Outline each blood parasite and name the species.
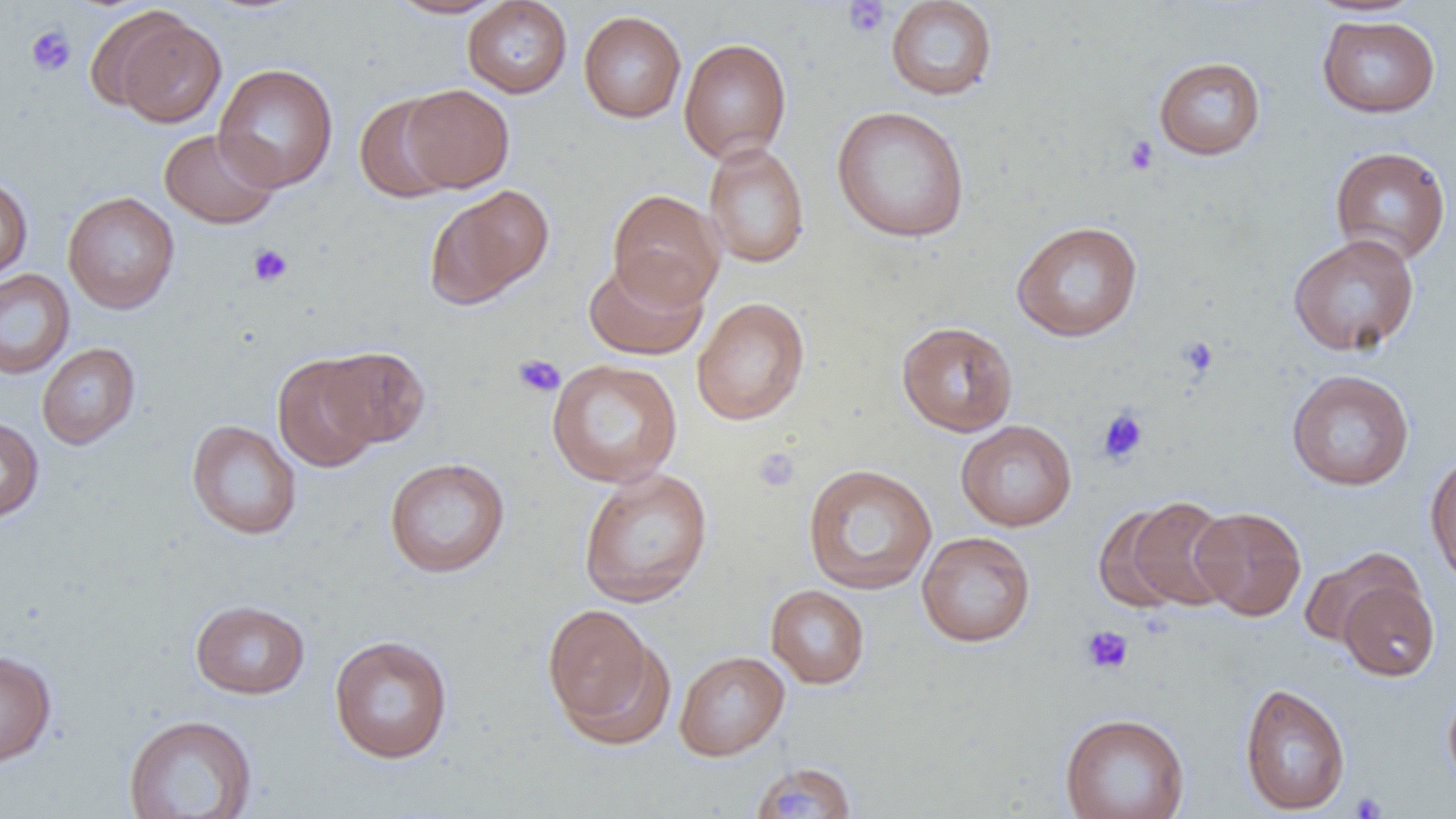
No blood parasites observed.

Summary:
  - Coordinate format: approximate bounding boxes as (x1,y1)-(x2,y2) corner pairs in pixels
  - Uninfected red blood cell locations: (385,0)-(509,19), (885,0)-(998,101), (462,1)-(572,98), (578,11)-(686,123), (111,14)-(226,128), (1317,15)-(1440,118), (678,37)-(793,163), (1153,56)-(1266,160), (213,63)-(338,192), (402,84)-(514,192), (354,92)-(459,203), (831,105)-(970,243), (159,127)-(281,229), (703,141)-(810,269), (1330,146)-(1451,265), (0,174)-(32,282), (426,184)-(555,308), (607,189)-(725,309), (62,191)-(179,315), (1011,220)-(1143,342), (1288,233)-(1420,357), (583,255)-(709,361), (0,269)-(75,380), (691,297)-(810,426), (896,320)-(1018,437), (37,343)-(140,450), (317,346)-(430,448), (272,353)-(383,472), (546,358)-(683,488), (1286,369)-(1415,491), (0,416)-(44,522), (186,420)-(302,540), (955,420)-(1077,531), (1424,452)-(1456,585), (384,457)-(510,578), (802,463)-(937,595), (577,467)-(714,608), (1106,495)-(1237,612), (1190,506)-(1307,620), (916,531)-(1036,647), (1298,547)-(1422,648), (1337,578)-(1440,681), (765,584)-(870,689), (190,599)-(311,699), (541,603)-(670,743), (328,635)-(453,764), (0,649)-(58,768), (674,650)-(790,761), (1442,681)-(1456,794), (1239,682)-(1351,815), (1059,712)-(1190,819), (123,713)-(257,818), (750,762)-(856,819)
  - Platelet locations: (843,0)-(890,38), (25,24)-(76,77), (1123,135)-(1158,176), (247,243)-(293,287), (1177,335)-(1219,379), (513,353)-(565,398), (1097,408)-(1149,465), (753,446)-(801,493), (1081,625)-(1134,675), (1349,791)-(1387,818)
  - Slide-level diagnosis: negative for blood parasites
  - Magnification: 1000x
  - Image size: 1456×819 pixels
  - Modality: optical microscopy
  - Field of view: single
  - Preparation: thin blood smear